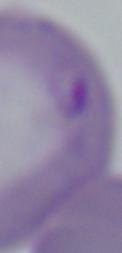

Summary:
  - Modality: photomicrograph
  - Magnification: 1000x
  - Identification: Babesia